State which parasite is depicted.
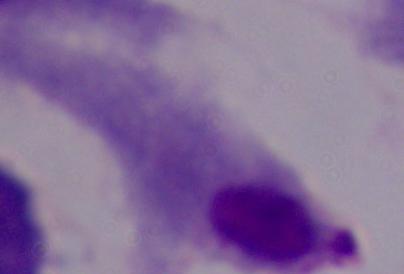
A trichomonad.

magnification = 1000x
modality = micrograph